Point out each leukocyte.
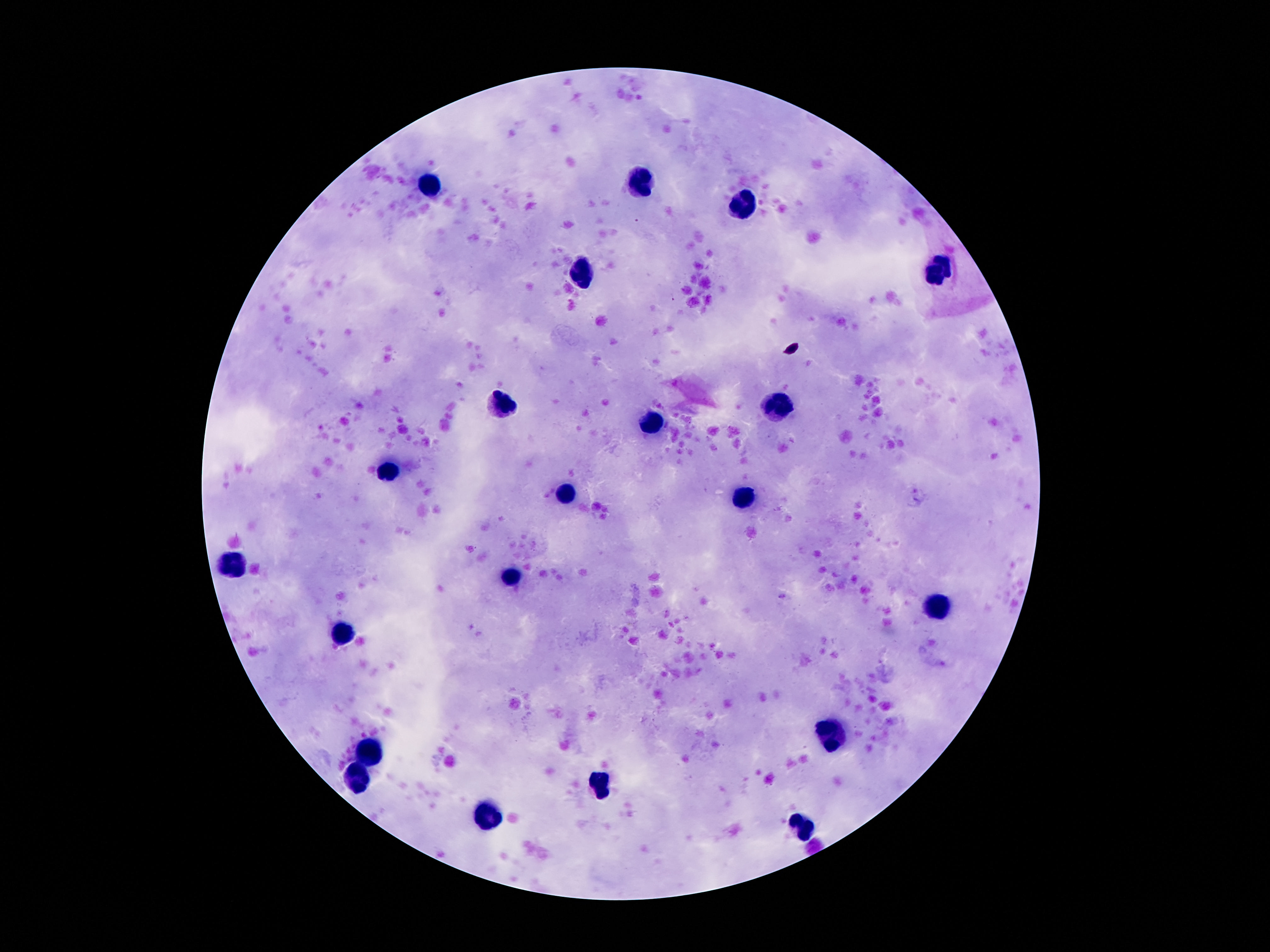
Approximate centers as (x, y) in pixels.
Leukocytes: (429, 183), (641, 184), (741, 204), (942, 267), (583, 269), (501, 397), (776, 404), (653, 424), (391, 469), (564, 495), (741, 499), (230, 564), (510, 576), (940, 607), (345, 633), (830, 732), (368, 753), (359, 779), (604, 788), (487, 816), (804, 823).

Single field of view. Giemsa stain. Image is 1270×952 pixels. Patient malaria status: not infected. Smartphone photograph taken through the microscope eyepiece. Thick blood smear. 100x magnification.